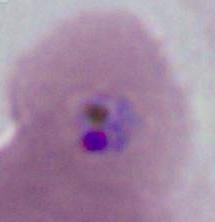

modality = micrograph
identification = Plasmodium
magnification = 400x or 1000x